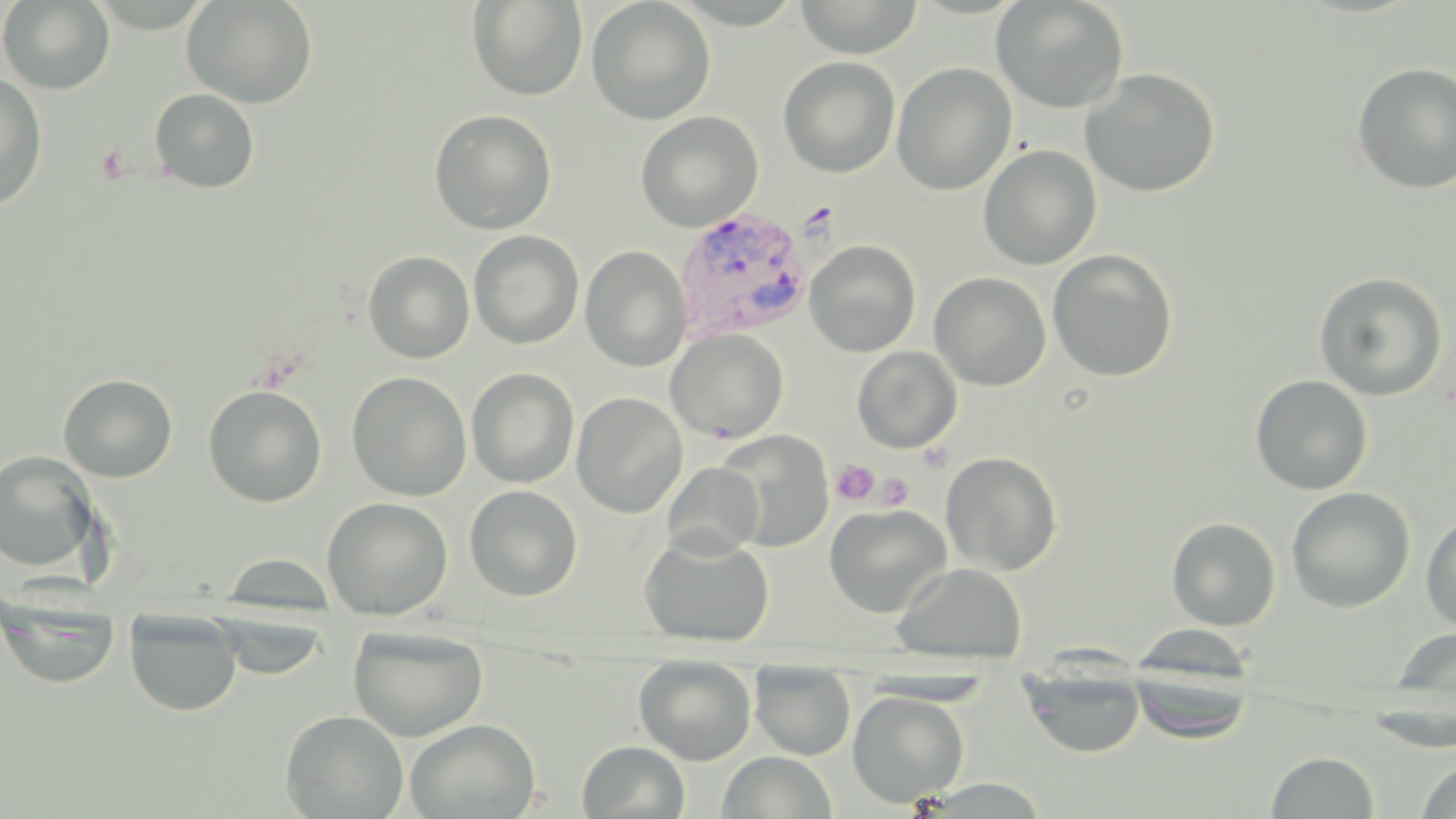

Approximate bounding boxes as (x1,y1)-(x2,y2) corner pairs in pixels. Plasmodium vivax-infected red blood cell locations: (674,208)-(813,342). Uninfected red blood cell locations: (0,0)-(115,94), (182,0)-(318,109), (467,0)-(587,101), (586,0)-(716,125), (794,0)-(924,59), (991,0)-(1130,114), (778,56)-(900,177), (1351,62)-(1456,195), (891,63)-(1016,196), (1080,68)-(1220,197), (0,71)-(47,210), (150,89)-(260,193), (429,109)-(557,234), (635,111)-(763,232), (978,144)-(1102,270), (468,230)-(584,350), (805,240)-(921,357), (580,245)-(690,372), (1046,249)-(1178,382), (363,250)-(475,363), (929,271)-(1051,391), (1314,271)-(1448,400), (666,328)-(789,444), (852,346)-(962,453), (466,367)-(579,488), (346,371)-(472,501), (58,374)-(178,482), (1250,374)-(1373,495), (203,385)-(327,507), (571,392)-(688,518), (716,429)-(834,552), (1,451)-(101,572), (940,451)-(1062,575), (662,462)-(764,559), (465,484)-(583,601), (1286,486)-(1416,613), (322,497)-(453,620), (824,503)-(953,618), (1421,510)-(1456,635), (1167,516)-(1281,631), (638,532)-(775,648), (892,562)-(1028,664), (1,599)-(122,689), (207,610)-(330,681), (125,611)-(242,717), (348,625)-(488,742), (1389,628)-(1456,703), (634,658)-(757,766), (1018,664)-(1147,758), (1126,664)-(1259,743), (750,665)-(855,760), (848,691)-(969,808), (280,709)-(408,818), (405,719)-(540,818), (577,740)-(690,819), (1266,750)-(1380,818), (717,751)-(838,819), (1416,761)-(1456,818). Platelet locations: (95,144)-(133,185), (831,458)-(879,505), (875,473)-(913,511). Slide-level diagnosis: Plasmodium vivax. Image is 1456×819 pixels. May-Grünwald-Giemsa stain. Single field of view. 1000x magnification. Thin blood smear. Optical microscopy.